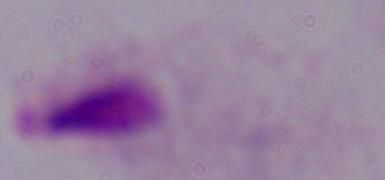

Photomicrograph. A trichomonad is shown. 1000x magnification.